Name the blood parasite species.
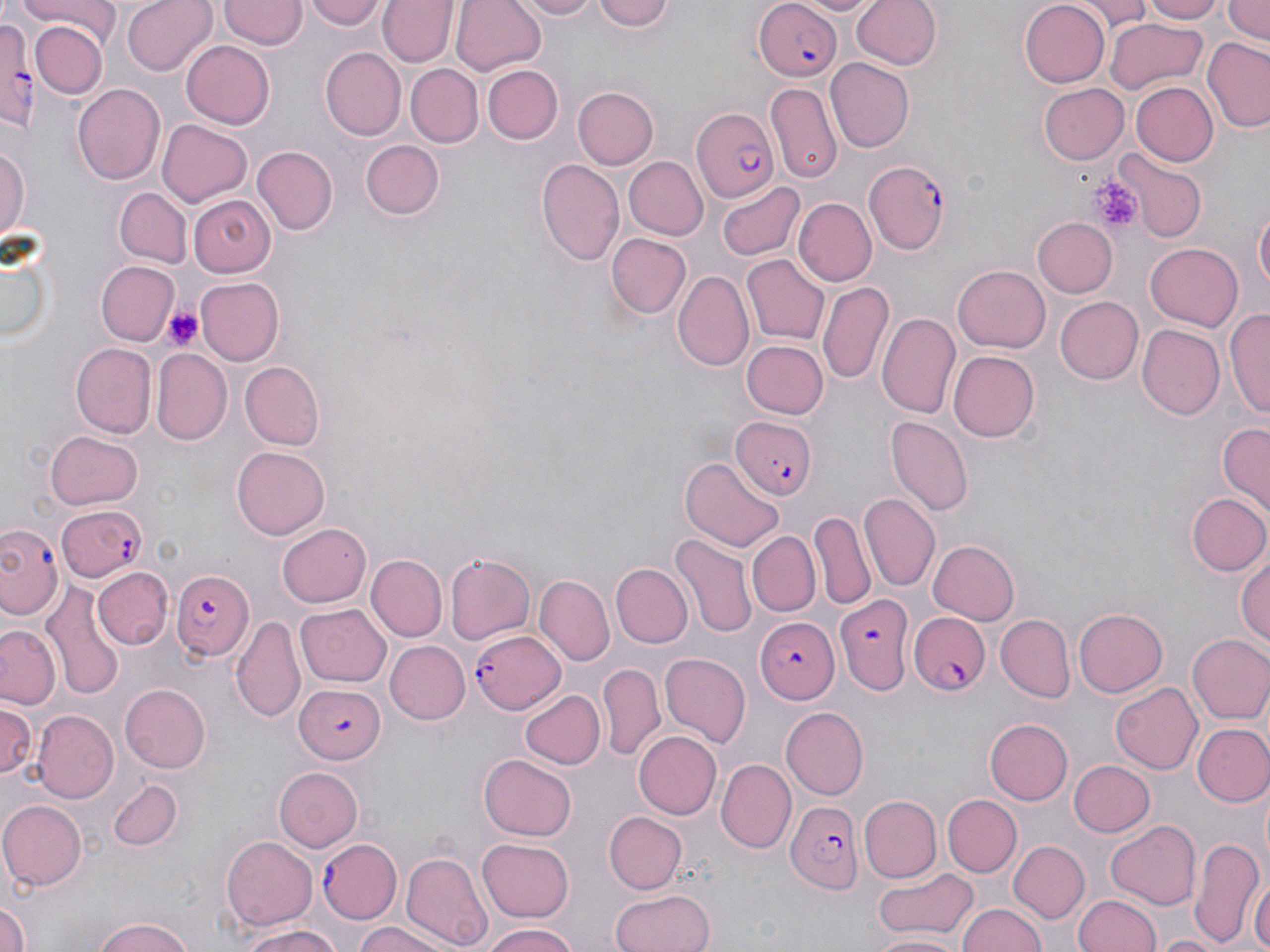
Plasmodium falciparum.

modality = light microscopy
image size = 1270×952 pixels
preparation = thin blood film
field of view = one of a larger specimen
magnification = 1000x
platelet locations = approximate bounding boxes as [x1, y1, x2, y2] in pixels: [1089, 175, 1143, 234], [163, 305, 204, 350]
stain = May-Grünwald-Giemsa
uninfected red blood cell locations = approximate bounding boxes as [x1, y1, x2, y2] in pixels: [15, 0, 119, 43], [122, 0, 216, 74], [220, 0, 304, 50], [301, 0, 385, 31], [379, 0, 457, 69], [451, 0, 546, 74], [511, 0, 605, 20], [595, 0, 673, 34], [795, 0, 878, 15], [851, 0, 942, 73], [1078, 0, 1150, 30], [1141, 0, 1225, 23], [1224, 0, 1270, 46], [1020, 1, 1110, 87], [1105, 16, 1207, 97], [31, 21, 106, 99], [1202, 37, 1270, 134], [184, 41, 274, 128], [320, 48, 405, 140], [824, 58, 914, 153], [407, 64, 484, 147], [482, 66, 562, 144], [1038, 82, 1129, 165], [1130, 82, 1220, 166], [765, 83, 843, 186], [72, 84, 166, 187], [571, 87, 656, 170], [158, 120, 251, 207], [362, 139, 445, 220], [0, 143, 30, 243], [251, 145, 337, 236], [1114, 151, 1206, 243], [621, 155, 706, 240], [535, 159, 624, 267], [717, 181, 803, 261], [114, 187, 191, 268], [723, 189, 876, 271], [189, 194, 274, 275], [793, 199, 875, 286], [1254, 203, 1269, 303], [1033, 218, 1117, 297], [605, 232, 690, 320], [0, 243, 56, 351], [1144, 243, 1244, 332], [741, 255, 831, 345], [96, 261, 177, 345], [953, 263, 1052, 353], [674, 270, 754, 371], [196, 277, 284, 366], [819, 284, 893, 386], [1056, 295, 1145, 385], [1228, 306, 1270, 420], [878, 309, 962, 416], [1136, 324, 1224, 421], [741, 339, 828, 420], [74, 343, 155, 435], [153, 348, 231, 443], [947, 350, 1038, 442], [238, 361, 324, 450], [885, 416, 972, 517], [1217, 422, 1269, 515], [43, 430, 142, 509], [231, 443, 329, 536], [678, 456, 783, 553], [1186, 492, 1270, 576], [859, 494, 940, 590], [811, 512, 875, 609], [279, 522, 372, 607], [748, 531, 820, 615], [671, 533, 757, 638], [928, 540, 1021, 626], [1235, 546, 1269, 652], [445, 554, 537, 643], [366, 555, 447, 642], [612, 564, 693, 647], [95, 567, 171, 647], [536, 574, 612, 664], [42, 583, 123, 701], [295, 605, 390, 687], [1074, 606, 1168, 696], [232, 615, 306, 724], [997, 615, 1074, 701], [1, 624, 61, 709], [1187, 634, 1270, 725], [385, 641, 469, 724], [659, 650, 751, 745], [598, 663, 665, 761], [1110, 683, 1202, 775], [120, 684, 210, 773], [520, 688, 603, 771], [1, 701, 38, 785], [782, 706, 872, 799], [31, 711, 117, 804], [985, 718, 1073, 804], [1195, 724, 1270, 806], [631, 731, 720, 820], [479, 755, 576, 840], [717, 758, 795, 854], [1069, 760, 1154, 837], [274, 768, 362, 851], [106, 780, 183, 852], [942, 794, 1019, 877], [857, 796, 941, 883], [1, 800, 86, 889], [602, 811, 686, 894], [1106, 820, 1201, 910], [221, 834, 318, 932], [1189, 835, 1262, 945], [477, 838, 576, 921], [408, 841, 565, 939], [1009, 841, 1090, 923], [402, 848, 491, 950], [873, 869, 979, 939], [1249, 874, 1270, 952], [609, 888, 716, 952], [1074, 894, 1163, 952], [0, 902, 31, 952], [957, 903, 1048, 952], [90, 917, 196, 952], [235, 921, 342, 952], [350, 921, 456, 952], [483, 924, 581, 952], [866, 932, 964, 951], [1153, 933, 1227, 952]
Plasmodium falciparum-infected red blood cell locations = approximate bounding boxes as [x1, y1, x2, y2] in pixels: [753, 1, 843, 81], [0, 13, 37, 125], [691, 108, 778, 202], [867, 162, 954, 257], [729, 413, 815, 502], [56, 503, 146, 581], [0, 525, 62, 622], [169, 569, 255, 661], [837, 593, 915, 693], [910, 612, 993, 696], [755, 617, 839, 703], [470, 628, 567, 713], [294, 683, 385, 761], [786, 802, 863, 895], [317, 838, 401, 922]